Identify the parasite.
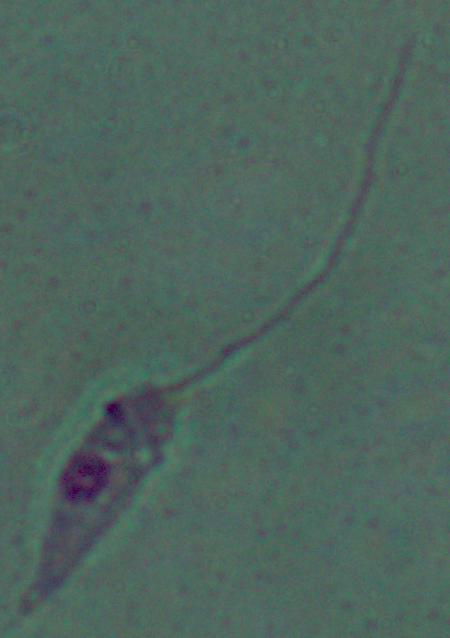

This is Leishmania.

magnification = 1000x
modality = photomicrograph